Identify the parasite.
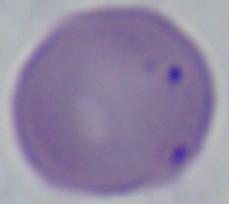
Babesia.

1000x magnification. Micrograph.